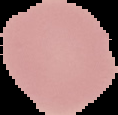
{
  "image_size": "118×115 pixels",
  "malaria_status": "uninfected",
  "preparation": "thin blood film",
  "image_type": "segmented cell region on a black background"
}